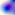

Summary:
  - Modality: micrograph
  - Magnification: 400x
  - Identification: Toxoplasma gondii